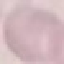
result = negative for malaria parasites
stain = Giemsa
preparation = thin blood film
capture = smartphone through the microscope eyepiece
image type = cell patch, automatically extracted from a larger field of view and resized to 64 × 64 pixels